Name the cell type shown.
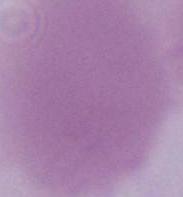

An erythrocyte.

modality = photomicrograph
magnification = 1000x